Name the parasite shown.
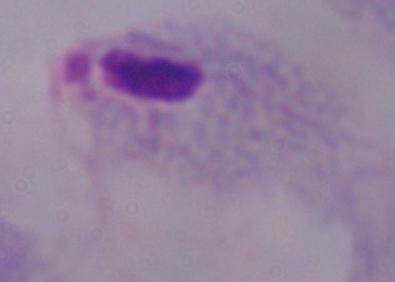

This is a trichomonad.

Captured at 1000x magnification. Photomicrograph.